Locate every blood parasite and identify its species.
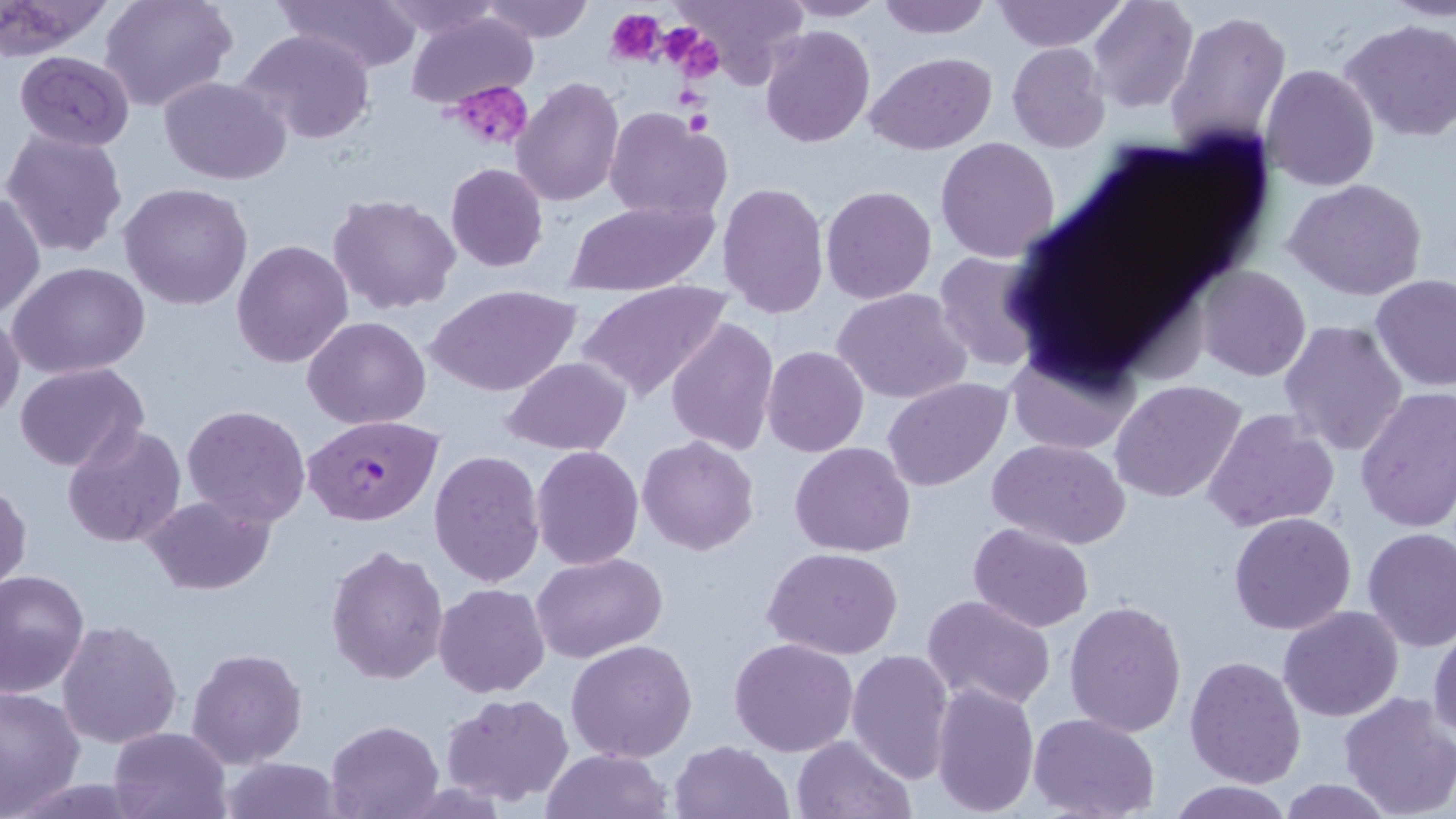

Approximate bounding boxes as [x1, y1, x2, y2] in pixels.
Plasmodium falciparum-infected red blood cells: [304, 414, 446, 525].
No Plasmodium ovale, Plasmodium malariae, Plasmodium vivax, Babesia divergens, or Trypanosoma brucei observed.

{
  "slide_level_diagnosis": "Plasmodium falciparum",
  "platelet_locations": "approximate bounding boxes as [x1, y1, x2, y2] in pixels: [607, 7, 666, 64], [657, 25, 718, 78], [451, 80, 533, 152], [683, 109, 711, 136]",
  "stain": "May-Grünwald-Giemsa",
  "preparation": "thin blood smear",
  "modality": "optical microscopy",
  "image_size": "1456×819 pixels",
  "uninfected_red_blood_cell_locations": "approximate bounding boxes as [x1, y1, x2, y2] in pixels: [99, 0, 236, 112], [281, 0, 422, 74], [377, 0, 508, 41], [672, 0, 809, 90], [779, 0, 890, 21], [875, 0, 994, 39], [995, 0, 1126, 52], [1088, 0, 1198, 115], [1388, 0, 1456, 20], [0, 1, 110, 56], [480, 1, 596, 42], [1164, 8, 1292, 155], [404, 10, 537, 110], [1340, 19, 1456, 142], [759, 24, 876, 148], [237, 27, 377, 147], [1007, 42, 1111, 153], [14, 50, 135, 151], [865, 52, 996, 155], [1259, 64, 1380, 192], [159, 76, 293, 184], [511, 76, 625, 207], [678, 104, 714, 141], [605, 105, 731, 223], [2, 127, 129, 260], [935, 136, 1059, 262], [444, 161, 549, 272], [1284, 178, 1428, 301], [716, 182, 830, 320], [119, 183, 253, 312], [820, 185, 938, 304], [1, 188, 44, 322], [327, 194, 461, 316], [565, 196, 719, 296], [231, 238, 354, 369], [931, 248, 1051, 373], [9, 262, 151, 381], [1195, 266, 1312, 381], [1370, 275, 1456, 392], [575, 279, 732, 406], [427, 283, 581, 398], [832, 288, 973, 404], [0, 310, 25, 425], [303, 315, 431, 428], [666, 317, 779, 457], [1279, 319, 1408, 456], [771, 341, 887, 556], [761, 346, 868, 457], [1006, 347, 1138, 455], [501, 356, 632, 456], [14, 362, 150, 473], [883, 378, 1012, 493], [1110, 380, 1247, 505], [1355, 389, 1456, 532], [181, 405, 312, 527], [1202, 408, 1340, 534], [62, 422, 186, 549], [638, 436, 760, 555], [989, 439, 1132, 550], [789, 441, 916, 558], [531, 444, 643, 570], [428, 450, 546, 587], [0, 479, 31, 598], [141, 494, 275, 594], [1228, 511, 1358, 636], [968, 522, 1095, 634], [1361, 527, 1456, 652], [324, 544, 450, 685], [763, 547, 904, 661], [532, 552, 667, 664], [1, 569, 91, 695], [432, 583, 551, 698], [923, 593, 1057, 710], [1062, 598, 1187, 738], [1278, 605, 1403, 721], [55, 619, 183, 749], [1429, 622, 1456, 744], [729, 636, 858, 756], [565, 639, 698, 763], [187, 647, 308, 768], [845, 648, 955, 783], [1185, 657, 1306, 789], [932, 680, 1040, 817], [0, 684, 86, 819], [1338, 691, 1456, 817], [440, 692, 574, 807], [1029, 713, 1161, 819], [324, 719, 445, 818], [107, 725, 232, 818], [791, 734, 915, 818], [670, 739, 793, 819], [540, 748, 671, 819], [217, 756, 348, 818], [1165, 779, 1291, 817], [1277, 779, 1395, 817]",
  "field_of_view": "single",
  "magnification": "1000x"
}